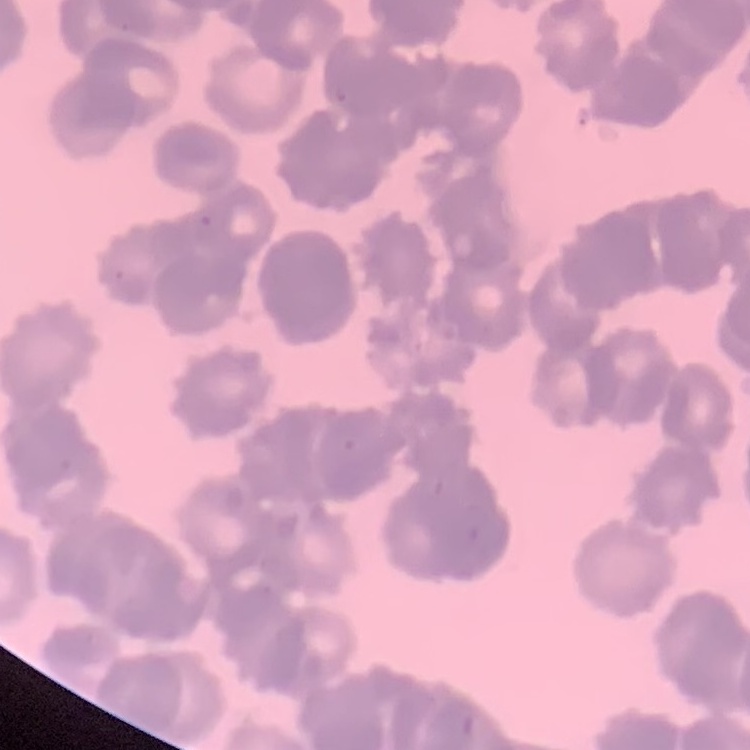 The erythrocytes show rouleaux formation. Thin peripheral smear. Field's or Giemsa stain. Square crop of a larger photomicrograph.